Describe the morphology of the red blood cells.
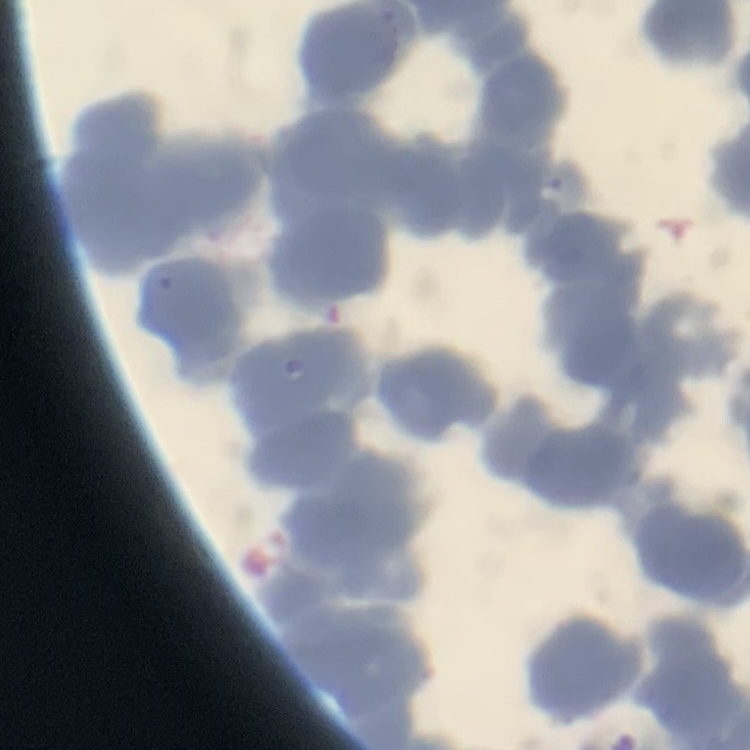
Rouleaux formation.

{
  "stain": "Field's or Giemsa",
  "image_type": "one tile cut from a larger photomicrograph",
  "preparation": "thin blood film"
}